Identify the cell.
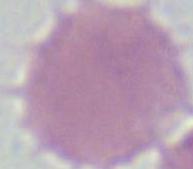

An erythrocyte.

{
  "modality": "photomicrograph",
  "magnification": "1000x"
}